Locate every Plasmodium parasite.
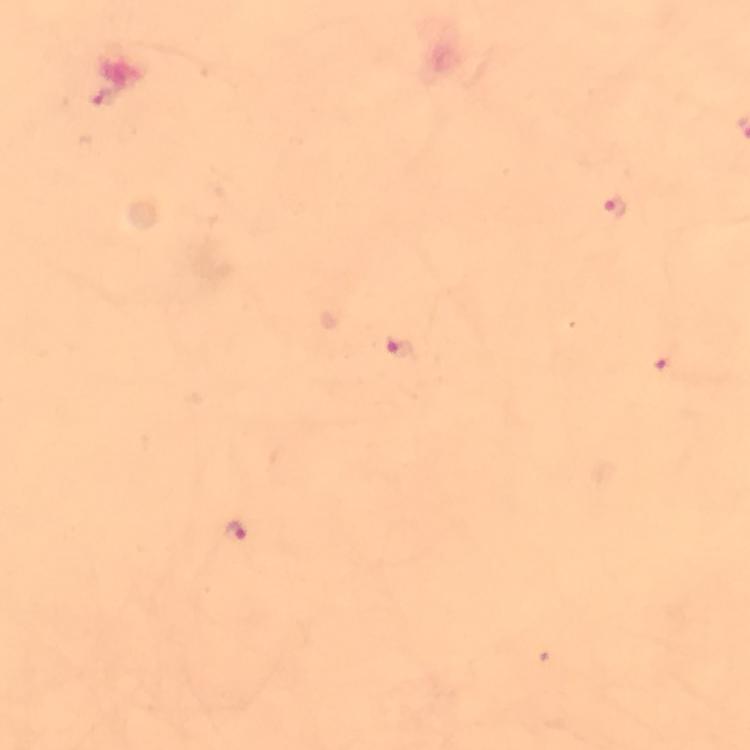

Approximate centers as {x, y} in pixels.
Plasmodium parasites: {105, 98}, {615, 207}, {398, 348}, {660, 360}, {236, 534}.

image_size: 750×750 pixels
magnification: 100x
stain: Giemsa
preparation: thick blood smear
context: from a malaria diagnostic workup
immersion_oil: used
capture: smartphone photograph through a microscope
cropped_from: one field of view